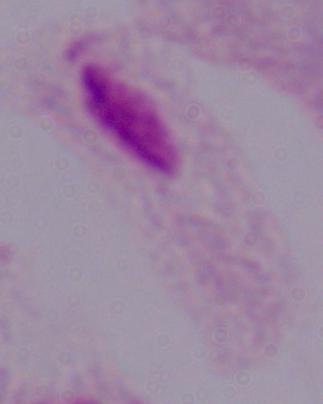

Summary:
  - Identification: trichomonad
  - Magnification: 1000x
  - Modality: micrograph